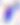

Toxoplasma gondii is shown. 400x magnification. Photomicrograph.